Point out each Plasmodium parasite.
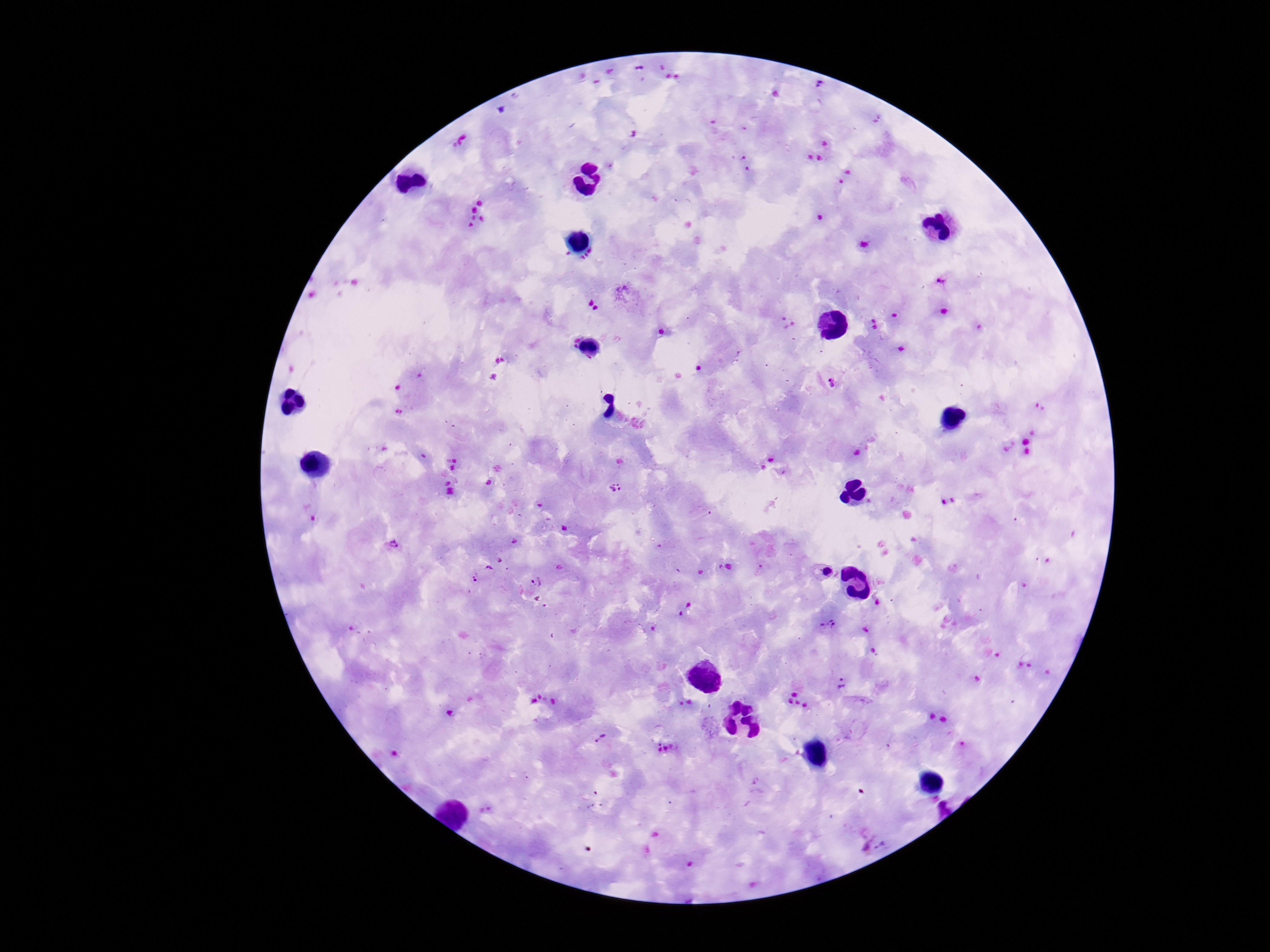

Approximate object centers, in pixels from the top-left corner.
Plasmodium parasites: (x=832, y=382), (x=615, y=487), (x=515, y=541), (x=393, y=545), (x=499, y=560), (x=488, y=570), (x=821, y=571), (x=475, y=579), (x=537, y=582), (x=877, y=603), (x=828, y=625), (x=864, y=630), (x=843, y=684), (x=600, y=739), (x=881, y=845).

capture = smartphone camera through the microscope eyepiece
preparation = thick peripheral-blood smear
patient malaria status = positive
field of view = single
magnification = 100x
stain = Giemsa
image size = 1270×952 pixels